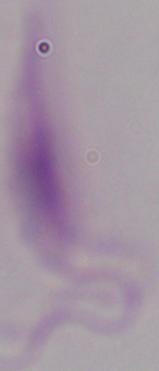

modality = micrograph
identification = Leishmania
magnification = 1000x